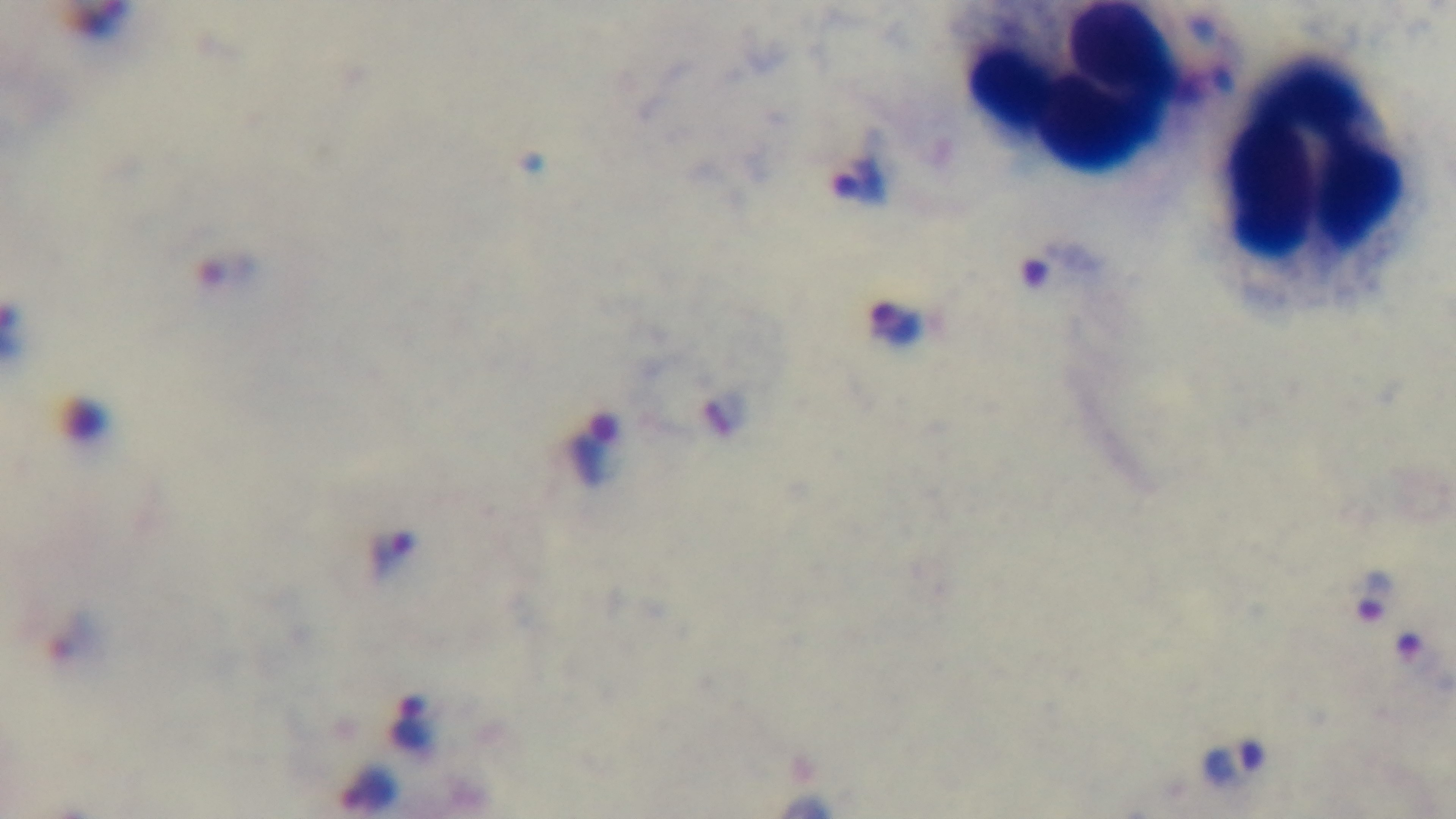

Summary:
  - Malaria status: positive
  - Objective: 100x oil immersion
  - Stain: Giemsa
  - Preparation: thick smear
  - Field of view: single
  - Capture: mounted 4K digital camera
  - Modality: light microscopy